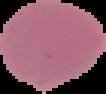
Summary:
  - Image size: 106×94 pixels
  - Preparation: thin blood film
  - Malaria status: uninfected
  - Image type: segmented cell region with the area outside set to black